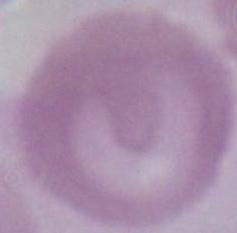
Summary:
  - Identification: red blood cell
  - Modality: photomicrograph
  - Magnification: 1000x